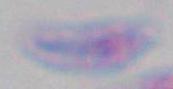
Summary:
  - Modality: micrograph
  - Magnification: 1000x
  - Identification: Toxoplasma gondii